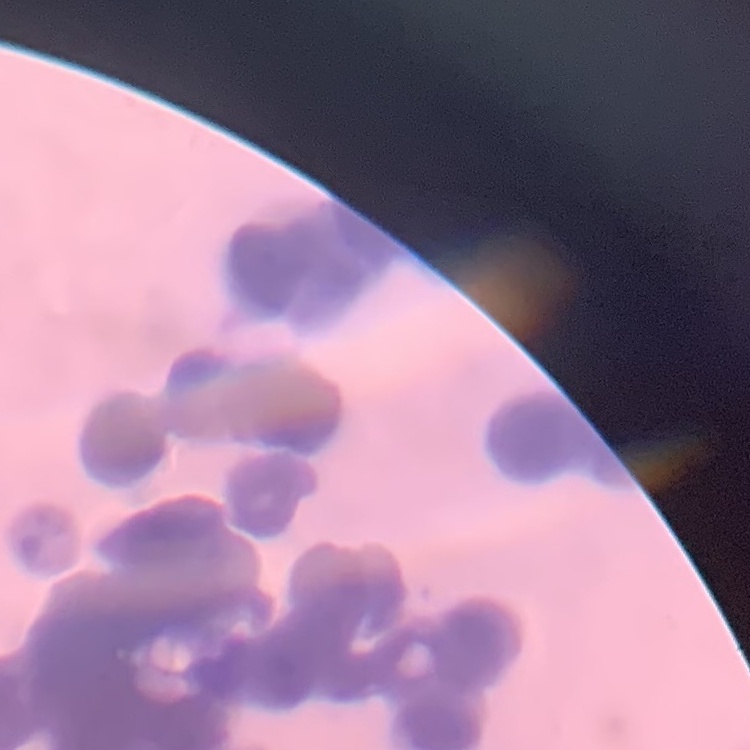
Summary:
  - Erythrocyte morphology: rouleaux formation
  - Stain: Field's or Giemsa
  - Preparation: thin blood film
  - Image type: square crop of a larger photomicrograph